Give the position of every Plasmodium parasite.
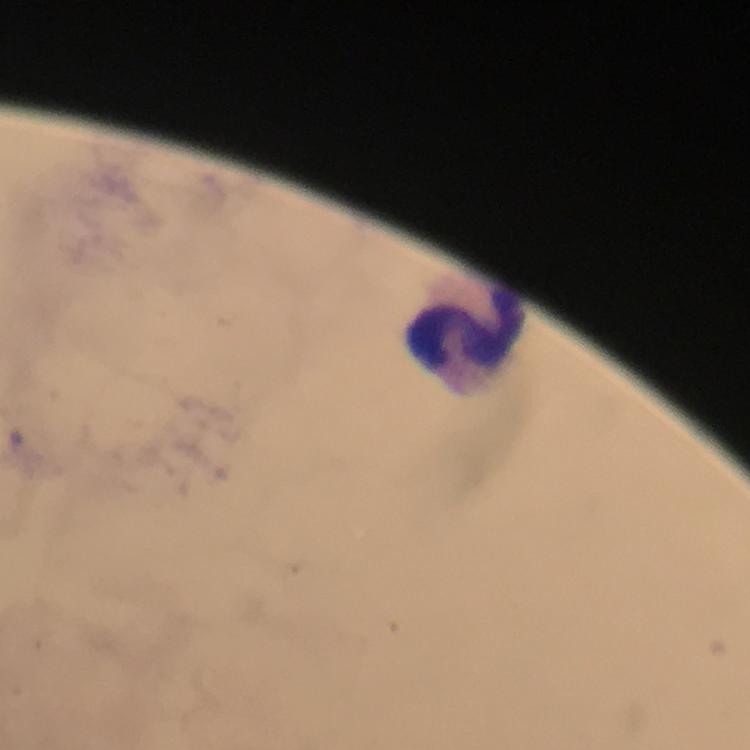

No Plasmodium parasites detected.

Approximate centers as {x, y} in pixels. Leukocyte locations: {468, 335}. Image is 750×750 pixels. Photographed with a smartphone mounted on the microscope. Thick smear. A crop from one field of view. At 100x magnification. From a malaria diagnostic workup. Giemsa stain. Immersion oil applied.